Name the blood parasite species.
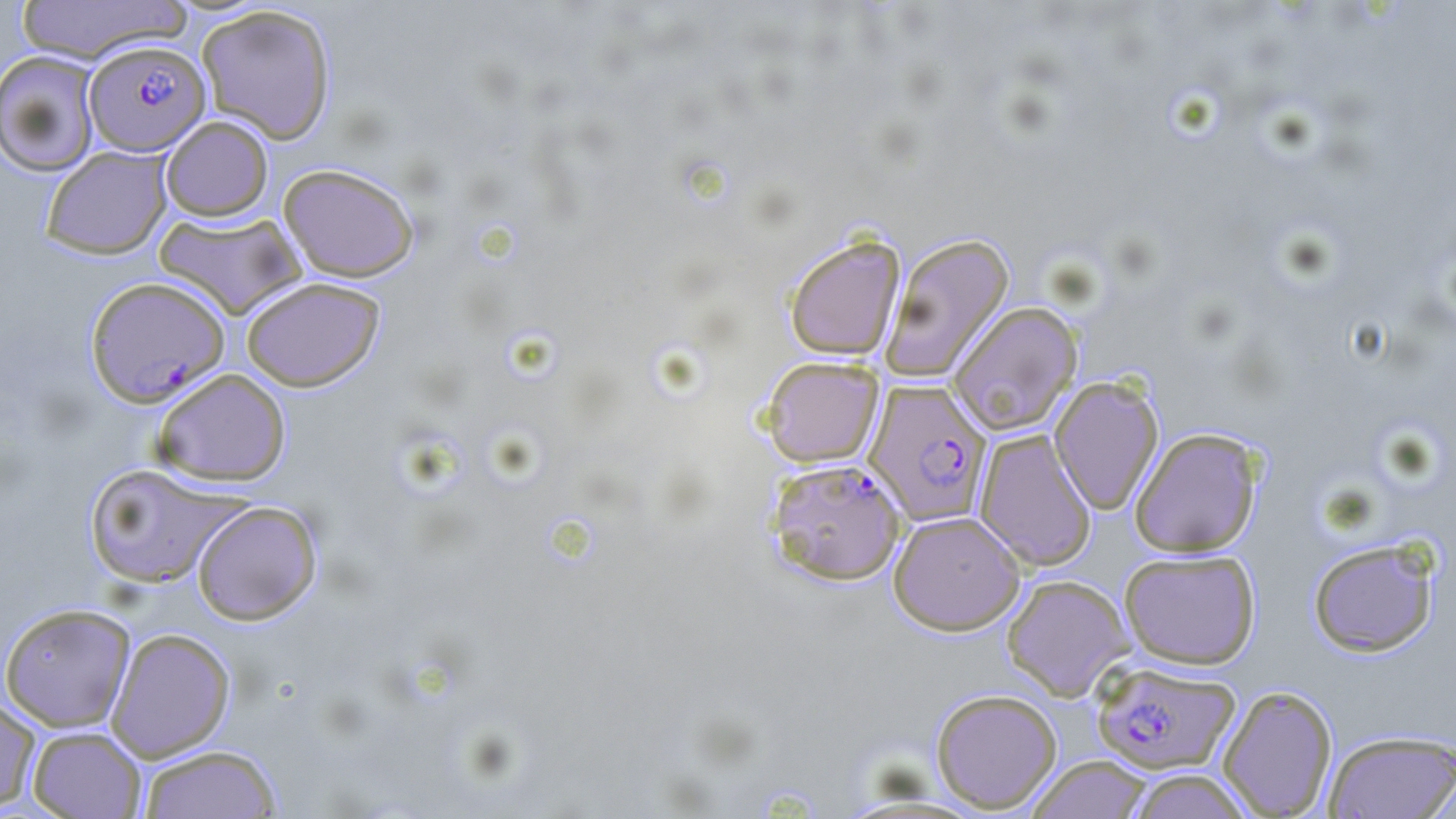

Plasmodium falciparum.

Approximate bounding boxes as [x1, y1, x2, y2] in pixels. Uninfected red blood cell locations: [16, 0, 190, 65], [195, 5, 337, 145], [0, 50, 103, 176], [160, 115, 273, 221], [41, 146, 172, 259], [278, 162, 420, 282], [153, 211, 306, 320], [881, 232, 1015, 383], [784, 234, 905, 361], [241, 276, 384, 391], [947, 301, 1083, 435], [761, 356, 884, 468], [152, 368, 291, 487], [1049, 376, 1164, 515], [1129, 428, 1262, 557], [974, 429, 1097, 570], [82, 462, 244, 589], [192, 500, 322, 625], [888, 510, 1025, 635], [1307, 538, 1440, 657], [1118, 549, 1261, 669], [1001, 574, 1135, 700], [0, 603, 136, 732], [106, 627, 236, 761], [1217, 684, 1338, 818], [930, 688, 1062, 813], [0, 697, 41, 812], [27, 726, 147, 819], [1323, 729, 1456, 819], [137, 744, 284, 818], [1027, 755, 1154, 818], [1125, 769, 1254, 818]. Plasmodium falciparum-infected red blood cell locations: [83, 39, 211, 156], [85, 275, 230, 407], [864, 380, 992, 527], [765, 457, 907, 586], [1091, 660, 1240, 774]. Thin blood film. May-Grünwald-Giemsa stain. Image is 1456×819 pixels. 1000x magnification. One field of a larger specimen. Light microscopy.